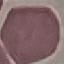
Result: negative for malaria parasites. Automatically extracted cell patch, resized to 64 × 64 pixels. Thin smear of blood. Giemsa-stained preparation. Photographed with a smartphone camera at the microscope eyepiece.